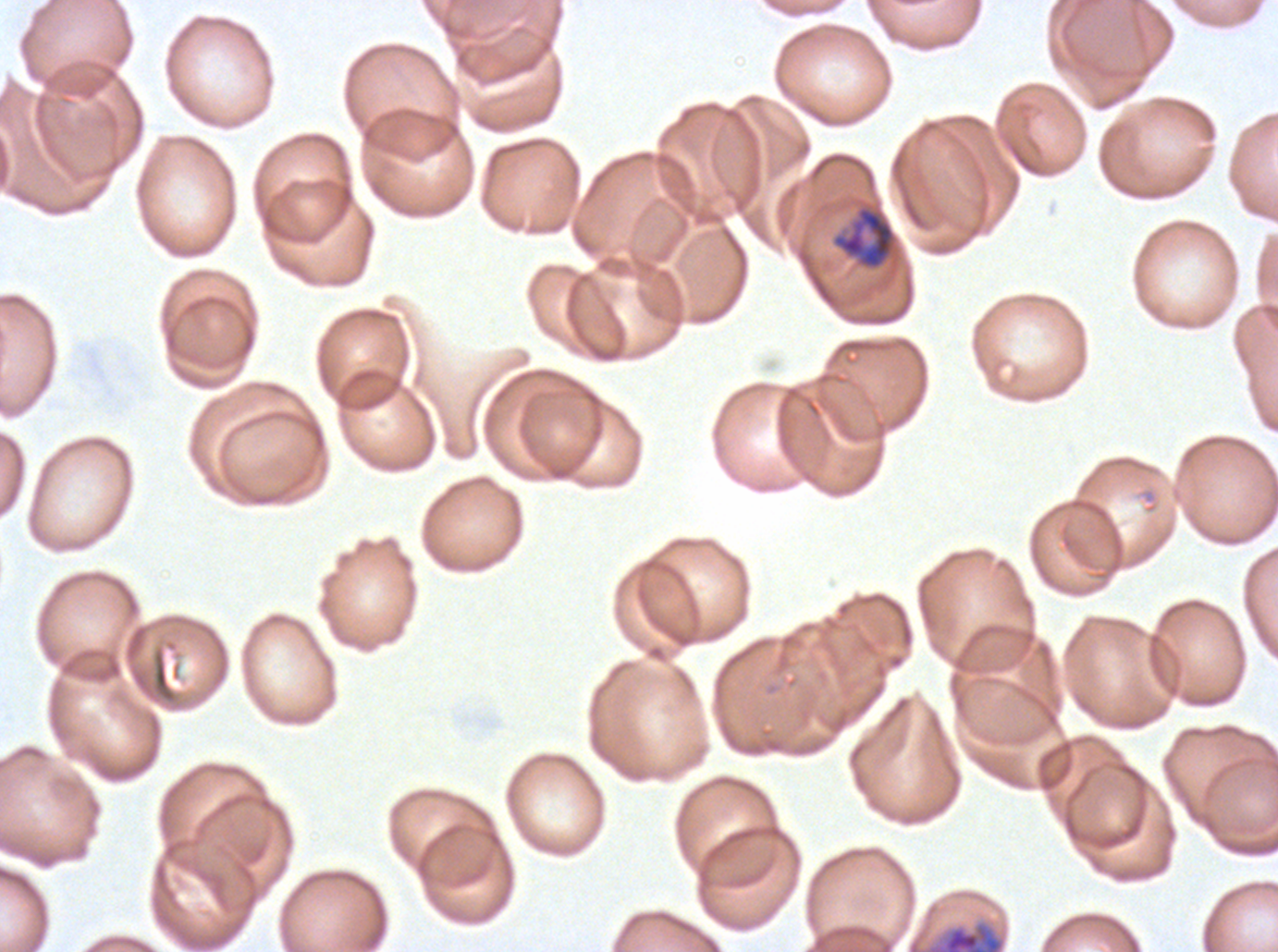
notation = approximate bounding rectangles given as corner coordinates in pixels from the top-left
mid trophozoite locations = (x1=831, y1=204, x2=897, y2=271)
early schizont locations = (x1=926, y1=921, x2=1005, y2=951)
life-cycle stages observed = mid trophozoite, early schizont
stain = Giemsa
specimen = P. falciparum cultured ex vivo for 24 to 48 hours, from a patient in The Gambia
field of view = one sub-image of a larger composite
preparation = thin blood smear
image size = 1278×952 pixels